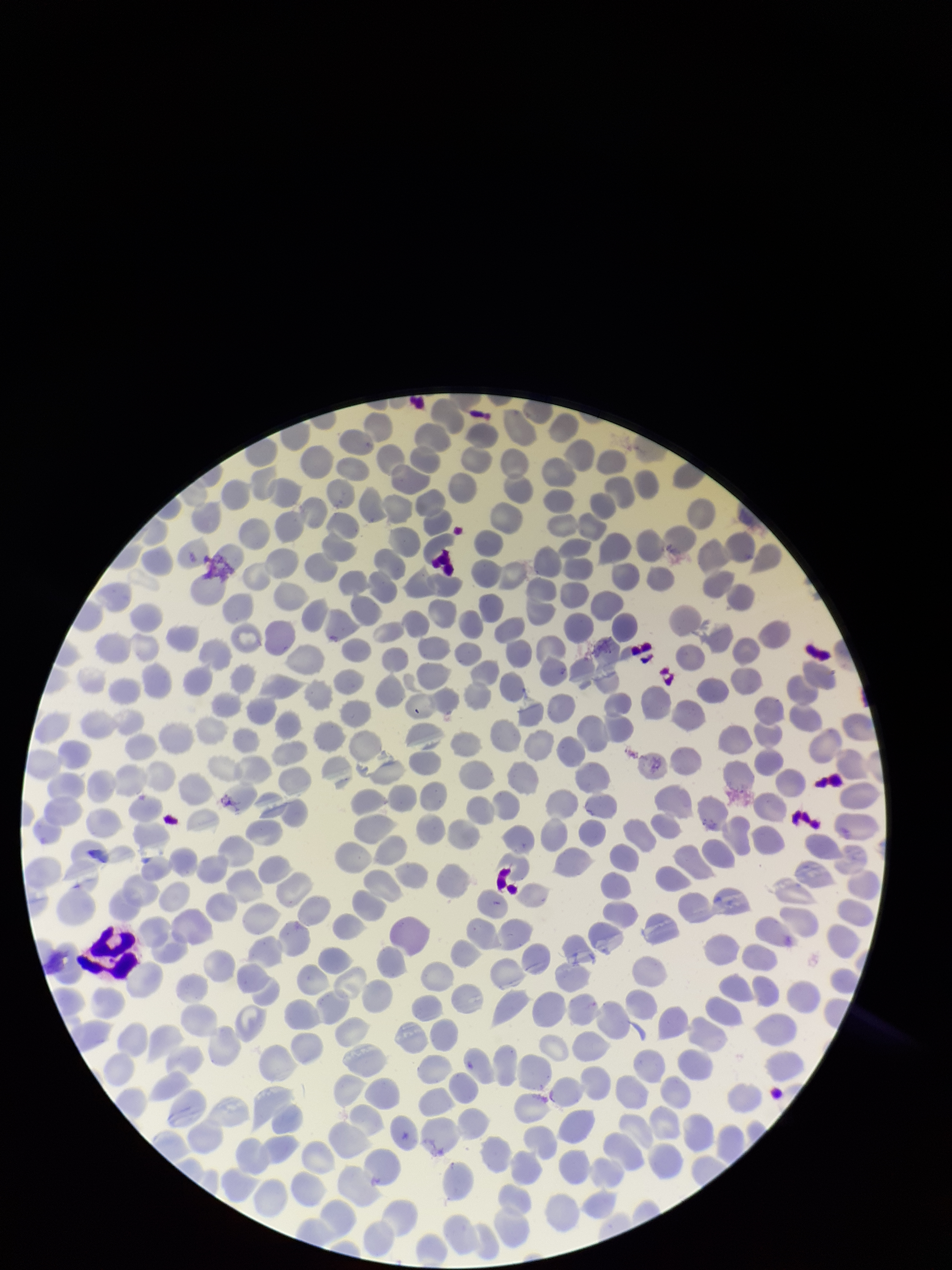

Summary:
  - Capture: smartphone photograph through the microscope eyepiece
  - Field of view: single
  - Patient malaria status: negative
  - Stain: Giemsa
  - Parasitized red blood cells: none detected
  - Parasitized red blood cell count: 0
  - Preparation: thin
  - Image size: 952×1270 pixels
  - Red blood cell count: 240